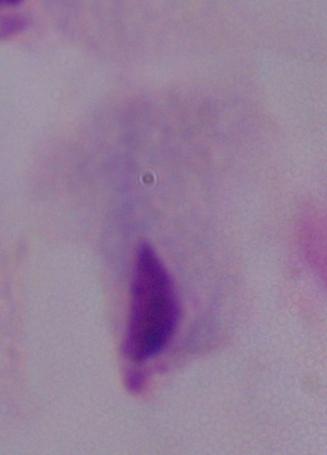
modality = photomicrograph
magnification = 1000x
identification = trichomonad